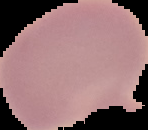

image size = 148×130 pixels
preparation = thin blood film
result = negative for Plasmodium parasites
image type = segmented cell region with the area outside set to black